Classify this cell by malaria status.
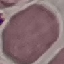

Uninfected.

Summary:
  - Image type: automatically extracted cell patch, resized to 64 × 64 pixels
  - Preparation: thin blood film
  - Stain: Giemsa
  - Capture: smartphone through the microscope eyepiece